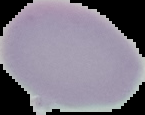
From a thin blood smear. Malaria status: uninfected. The area outside the segmented cell region is set to black. Image is 145×115 pixels.